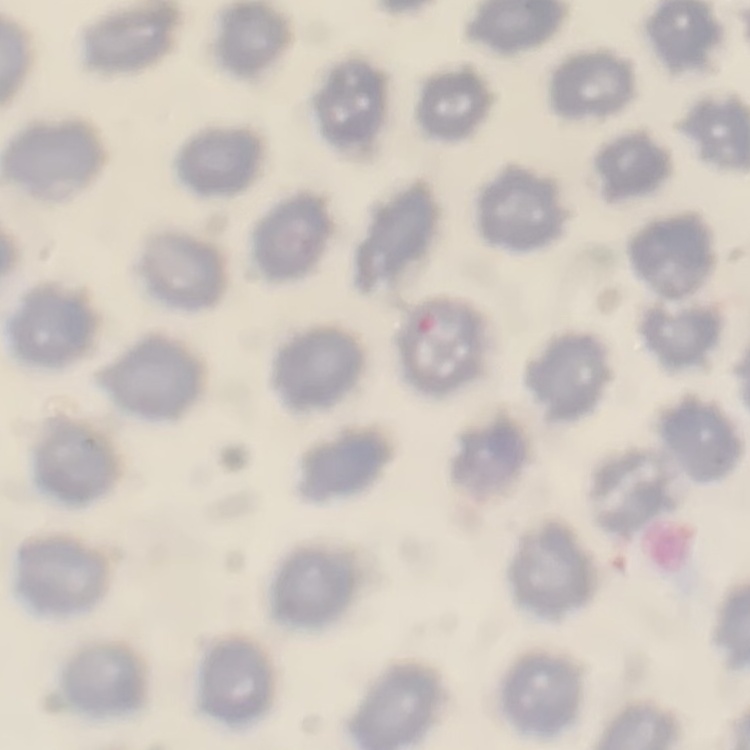

Summary:
  - Red blood cell morphology: no rouleaux formation
  - Preparation: thin peripheral smear
  - Image type: one tile cut from a larger photomicrograph
  - Stain: Field's or Giemsa